Describe the morphology of the erythrocytes.
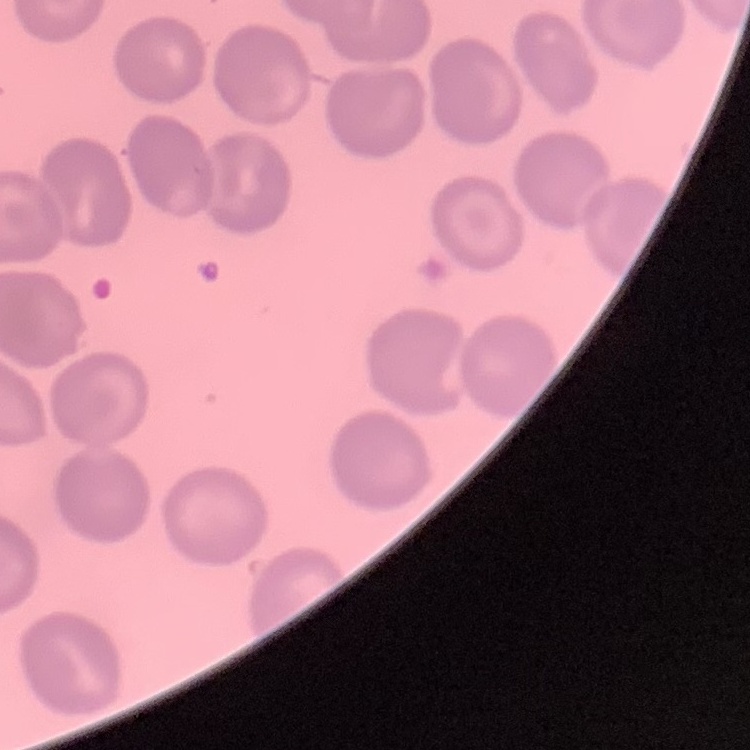

No rouleaux formation.

{
  "preparation": "thin blood film",
  "image_type": "square crop of a larger photomicrograph",
  "stain": "Field's or Giemsa"
}